Outline each Plasmodium malariae-infected red blood cell.
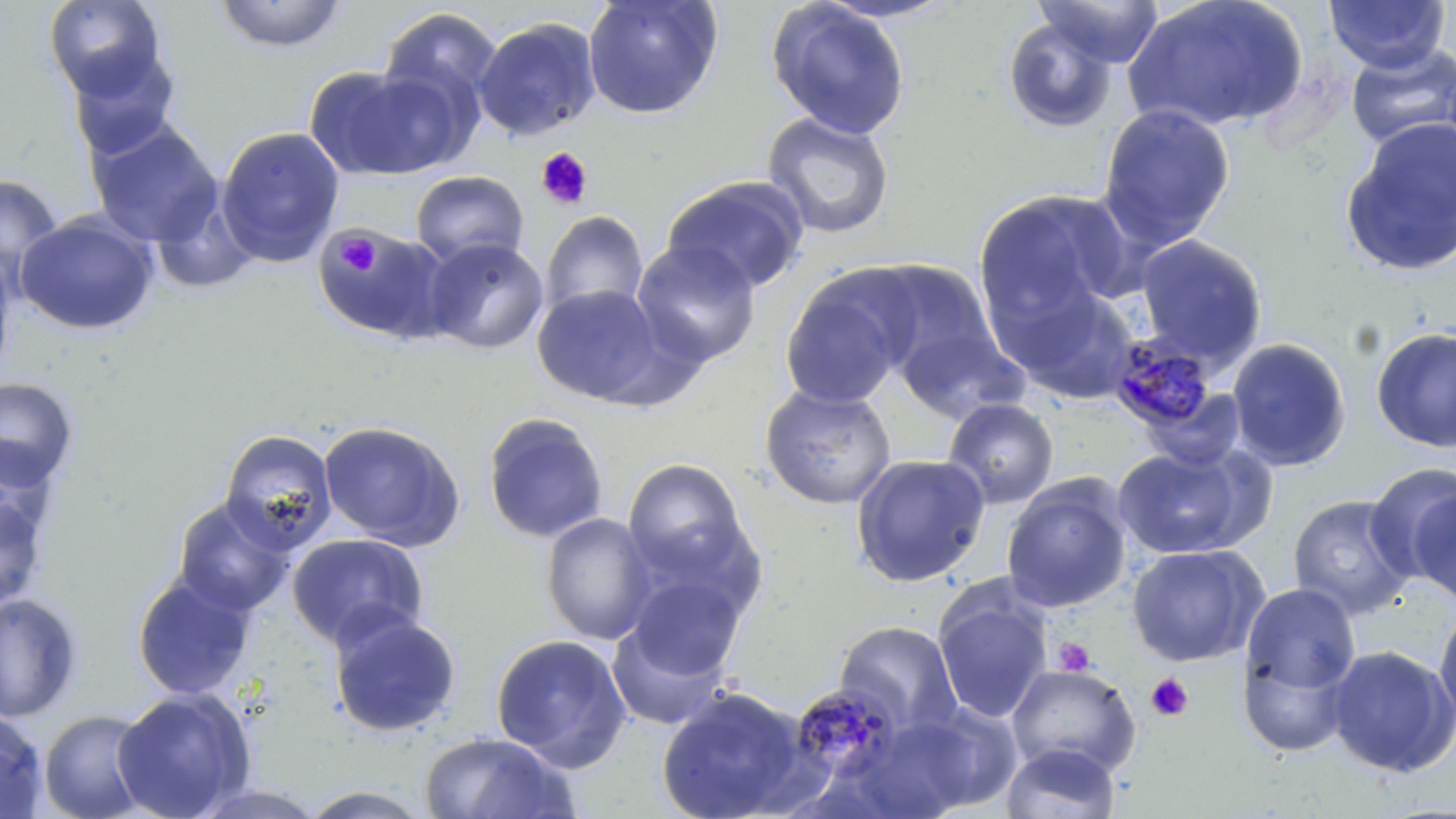

Approximate bounding boxes as named x1/y1/x2/y2 corners in pixels.
Plasmodium malariae-infected red blood cells: (x1=1103, y1=333, x2=1222, y2=438), (x1=789, y1=683, x2=904, y2=788).

Summary:
  - Platelet locations: (x1=536, y1=146, x2=593, y2=210), (x1=335, y1=233, x2=381, y2=277), (x1=1052, y1=636, x2=1096, y2=677), (x1=1146, y1=673, x2=1193, y2=721)
  - Uninfected red blood cell locations: (x1=43, y1=0, x2=167, y2=99), (x1=582, y1=0, x2=723, y2=120), (x1=766, y1=0, x2=912, y2=140), (x1=811, y1=0, x2=963, y2=24), (x1=1032, y1=0, x2=1165, y2=67), (x1=1123, y1=0, x2=1311, y2=136), (x1=1323, y1=0, x2=1451, y2=74), (x1=213, y1=1, x2=348, y2=53), (x1=377, y1=7, x2=504, y2=127), (x1=1002, y1=17, x2=1118, y2=135), (x1=473, y1=18, x2=602, y2=142), (x1=1344, y1=42, x2=1456, y2=153), (x1=66, y1=47, x2=183, y2=163), (x1=303, y1=64, x2=461, y2=182), (x1=1097, y1=103, x2=1236, y2=251), (x1=761, y1=111, x2=896, y2=240), (x1=85, y1=119, x2=223, y2=247), (x1=1338, y1=119, x2=1456, y2=278), (x1=215, y1=126, x2=345, y2=267), (x1=410, y1=170, x2=529, y2=270), (x1=0, y1=174, x2=63, y2=290), (x1=660, y1=175, x2=809, y2=295), (x1=973, y1=189, x2=1134, y2=336), (x1=539, y1=210, x2=649, y2=320), (x1=16, y1=211, x2=159, y2=336), (x1=312, y1=225, x2=451, y2=343), (x1=1133, y1=233, x2=1269, y2=370), (x1=421, y1=237, x2=549, y2=355), (x1=631, y1=240, x2=762, y2=369), (x1=0, y1=246, x2=18, y2=386), (x1=861, y1=260, x2=1000, y2=383), (x1=780, y1=267, x2=916, y2=408), (x1=993, y1=272, x2=1141, y2=403), (x1=531, y1=283, x2=669, y2=407), (x1=894, y1=323, x2=1026, y2=424), (x1=1369, y1=325, x2=1456, y2=453), (x1=1226, y1=337, x2=1352, y2=472), (x1=0, y1=377, x2=80, y2=493), (x1=759, y1=383, x2=897, y2=510), (x1=942, y1=398, x2=1059, y2=509), (x1=482, y1=412, x2=609, y2=544), (x1=317, y1=420, x2=466, y2=551), (x1=219, y1=429, x2=338, y2=556), (x1=0, y1=435, x2=60, y2=548), (x1=1112, y1=443, x2=1265, y2=560), (x1=849, y1=452, x2=991, y2=587), (x1=621, y1=458, x2=752, y2=586), (x1=1364, y1=464, x2=1456, y2=592), (x1=1000, y1=477, x2=1132, y2=613), (x1=1406, y1=481, x2=1456, y2=607), (x1=0, y1=489, x2=49, y2=614), (x1=1287, y1=494, x2=1417, y2=619), (x1=172, y1=498, x2=295, y2=617), (x1=540, y1=512, x2=657, y2=645), (x1=286, y1=533, x2=429, y2=651), (x1=1126, y1=543, x2=1268, y2=667), (x1=624, y1=572, x2=746, y2=684), (x1=132, y1=573, x2=256, y2=701), (x1=1241, y1=582, x2=1361, y2=695), (x1=932, y1=584, x2=1053, y2=725), (x1=0, y1=592, x2=82, y2=724), (x1=1433, y1=600, x2=1456, y2=733), (x1=327, y1=612, x2=462, y2=738), (x1=606, y1=618, x2=734, y2=731), (x1=834, y1=620, x2=962, y2=737), (x1=490, y1=634, x2=632, y2=773), (x1=1236, y1=640, x2=1357, y2=758), (x1=1325, y1=645, x2=1456, y2=778), (x1=1006, y1=663, x2=1141, y2=778), (x1=656, y1=686, x2=813, y2=819), (x1=112, y1=688, x2=256, y2=819), (x1=866, y1=706, x2=1017, y2=819), (x1=0, y1=707, x2=49, y2=818), (x1=38, y1=709, x2=155, y2=819), (x1=418, y1=732, x2=580, y2=819), (x1=1000, y1=742, x2=1121, y2=819), (x1=187, y1=784, x2=330, y2=818), (x1=296, y1=785, x2=436, y2=818)
  - Slide-level diagnosis: Plasmodium malariae
  - Field of view: single
  - Modality: optical microscopy
  - Magnification: 1000x
  - Stain: May-Grünwald-Giemsa
  - Preparation: thin blood film
  - Image size: 1456×819 pixels